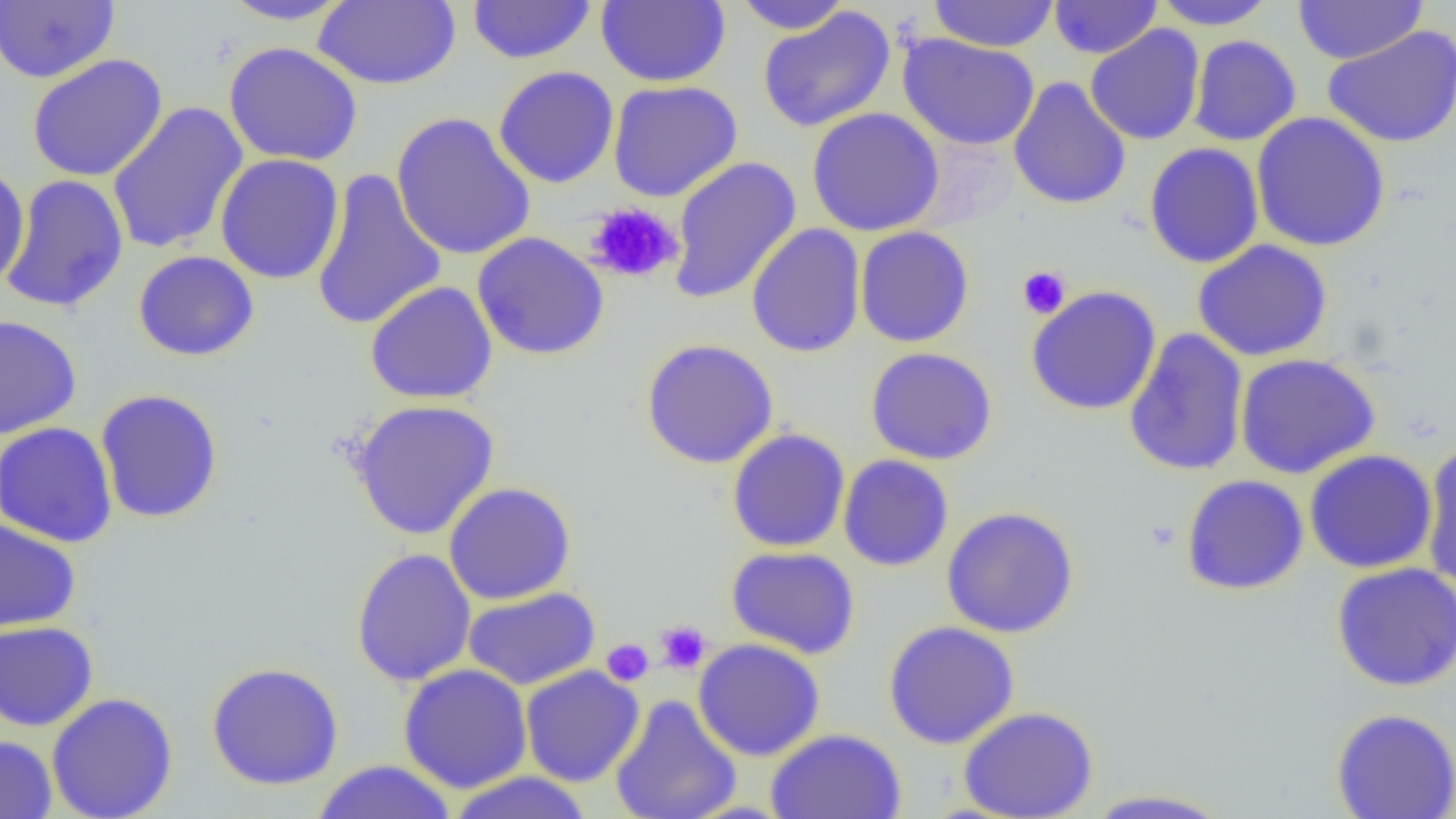

Summary:
  - Coordinate format: approximate bounding boxes as (x1, y1, x2, y2) in pixels
  - Platelet locations: (586, 201, 683, 284), (1017, 266, 1071, 319), (654, 620, 712, 675), (601, 638, 654, 687)
  - Uninfected red blood cell locations: (217, 0, 358, 25), (466, 0, 597, 65), (596, 0, 730, 87), (731, 0, 853, 35), (926, 0, 1060, 53), (1150, 0, 1278, 30), (1292, 0, 1429, 65), (0, 1, 119, 84), (314, 1, 461, 89), (1048, 1, 1161, 59), (757, 7, 896, 133), (1085, 24, 1205, 146), (1322, 26, 1456, 148), (898, 34, 1040, 150), (1187, 35, 1302, 146), (223, 42, 363, 166), (27, 54, 168, 183), (493, 66, 619, 188), (1008, 76, 1131, 210), (608, 80, 743, 202), (106, 101, 249, 256), (807, 107, 945, 237), (391, 112, 537, 261), (1250, 112, 1391, 252), (1144, 142, 1264, 268), (215, 153, 345, 284), (668, 156, 802, 304), (0, 163, 29, 291), (310, 168, 447, 333), (1, 174, 130, 313), (746, 223, 866, 358), (855, 226, 974, 348), (472, 232, 610, 360), (1192, 239, 1333, 362), (133, 250, 260, 361), (365, 281, 498, 404), (1026, 286, 1162, 415), (0, 315, 81, 439), (1123, 328, 1249, 477), (640, 338, 779, 469), (865, 346, 998, 466), (1234, 352, 1381, 479), (94, 389, 224, 523), (348, 399, 501, 540), (0, 421, 118, 548), (727, 429, 850, 552), (1421, 442, 1456, 595), (1303, 449, 1438, 574), (838, 454, 954, 572), (1180, 474, 1310, 596), (443, 482, 576, 605), (941, 506, 1079, 638), (0, 518, 80, 633), (726, 546, 861, 659), (350, 547, 477, 687), (1331, 562, 1456, 691), (463, 586, 600, 691), (0, 620, 98, 731), (883, 620, 1020, 749), (693, 638, 825, 761), (205, 661, 345, 791), (397, 663, 533, 793), (520, 666, 645, 787), (46, 692, 178, 818), (609, 694, 743, 819), (959, 706, 1098, 818), (1330, 708, 1456, 819), (765, 728, 907, 819), (0, 734, 57, 819), (311, 760, 458, 818), (445, 771, 596, 819), (1080, 788, 1237, 818)
  - Slide-level diagnosis: no evidence of blood parasites
  - Field of view: single
  - Modality: light microscopy
  - Preparation: thin blood smear
  - Magnification: 1000x
  - Image size: 1456×819 pixels